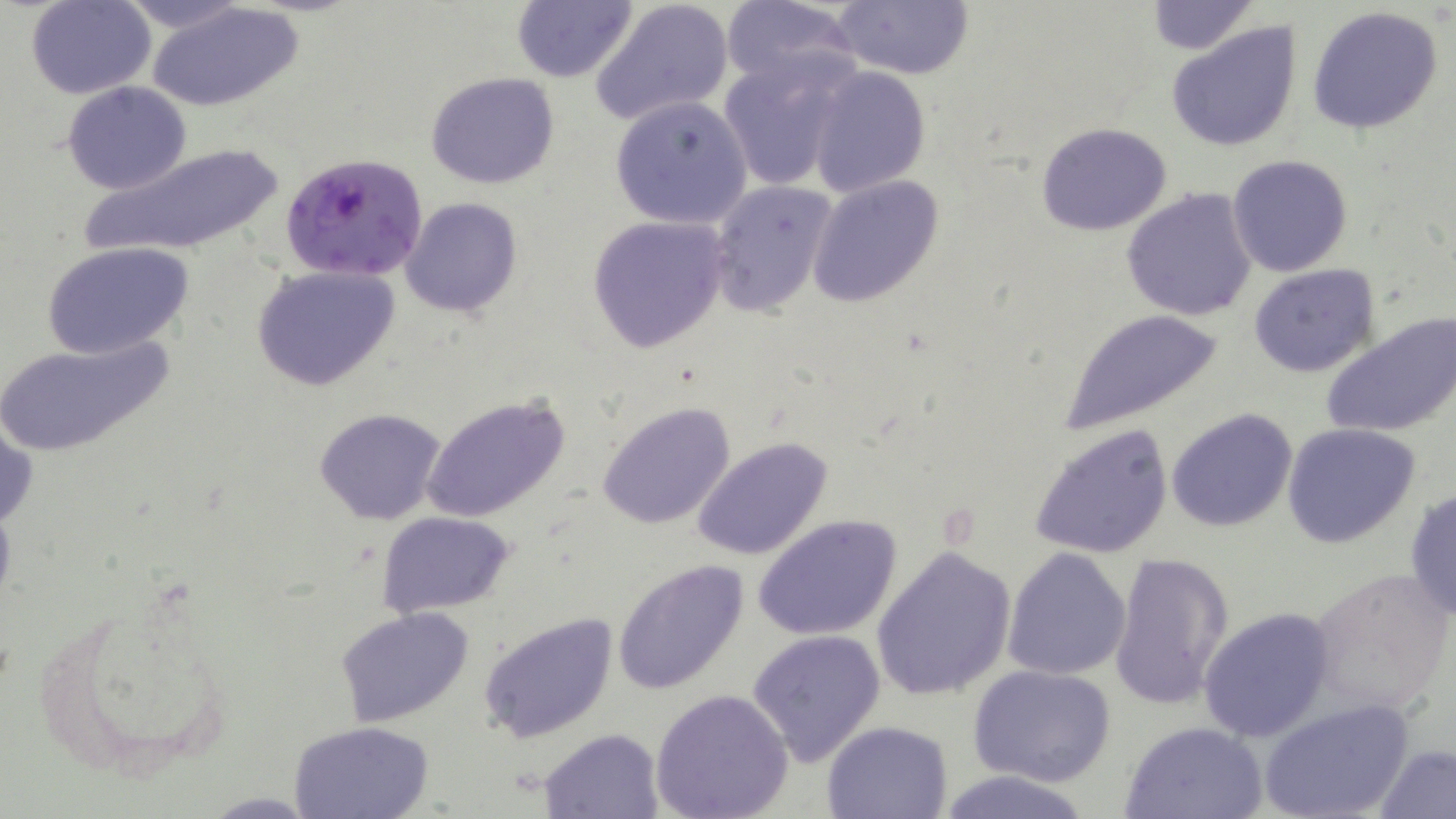
Summary:
  - Coordinate format: approximate bounding boxes as (x1,y1)-(x2,y2) corner pairs in pixels
  - Plasmodium falciparum-infected red blood cell locations: (280,153)-(428,283)
  - Uninfected red blood cell locations: (27,0)-(156,99), (113,0)-(257,37), (512,0)-(636,83), (721,0)-(862,92), (591,1)-(733,125), (830,1)-(974,81), (1145,2)-(1257,54), (150,3)-(303,112), (1305,6)-(1445,135), (1165,21)-(1302,153), (719,58)-(851,193), (806,65)-(931,196), (426,72)-(560,190), (63,81)-(192,195), (610,95)-(753,232), (1036,123)-(1173,236), (79,142)-(288,260), (1228,154)-(1352,277), (807,175)-(945,306), (708,180)-(837,317), (1121,188)-(1260,321), (399,198)-(522,317), (585,216)-(731,353), (41,242)-(194,360), (1248,263)-(1380,379), (250,264)-(403,393), (1058,311)-(1224,432), (1321,312)-(1456,439), (0,334)-(173,459), (420,393)-(572,522), (597,401)-(735,531), (1167,407)-(1298,532), (313,408)-(448,526), (1,413)-(36,533), (1027,422)-(1175,560), (1282,422)-(1422,547), (691,436)-(833,562), (1404,486)-(1456,622), (377,511)-(515,616), (756,515)-(902,642), (871,545)-(1015,700), (1004,548)-(1131,680), (1108,551)-(1234,710), (612,559)-(750,695), (1304,567)-(1454,717), (35,588)-(240,789), (333,605)-(478,728), (1199,606)-(1334,743), (478,612)-(620,744), (747,629)-(888,765), (970,666)-(1115,787), (649,688)-(794,819), (1261,697)-(1414,819), (289,719)-(435,819), (1118,719)-(1270,818), (822,720)-(952,818), (540,728)-(663,817), (1376,745)-(1455,819), (930,768)-(1099,819)
  - Slide-level diagnosis: Plasmodium falciparum
  - Preparation: thin blood film
  - Field of view: one of a larger specimen
  - Magnification: 1000x
  - Stain: May-Grünwald-Giemsa
  - Image size: 1456×819 pixels
  - Modality: light microscopy